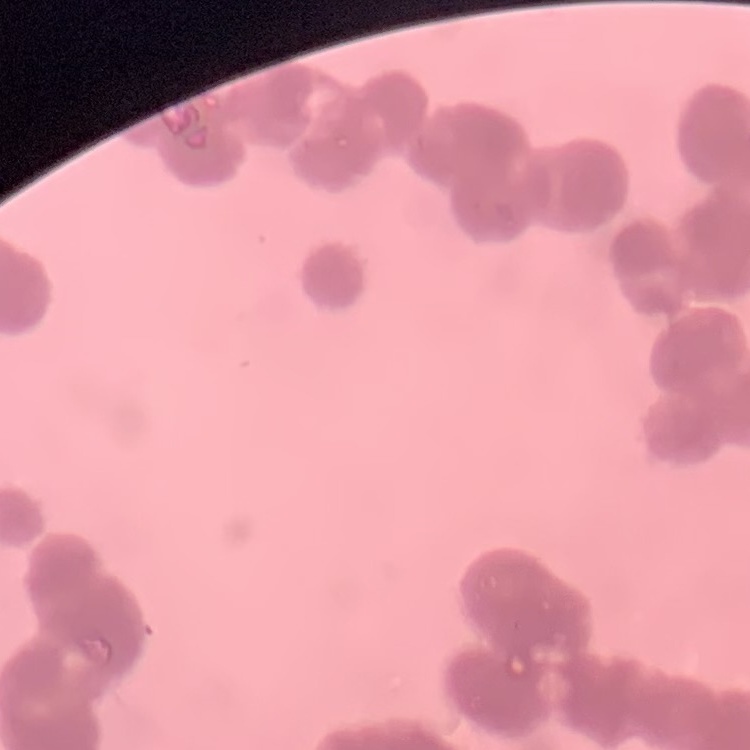 The red blood cells exhibit rouleaux formation. One tile cut from a larger photomicrograph. Thin blood film. Stained with either Field's or Giemsa.